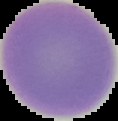

malaria status = uninfected
image size = 118×121 pixels
preparation = thin blood smear
image type = segmented cell region with the area outside set to black